Name the parasite shown.
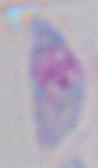
This is Toxoplasma gondii.

Summary:
  - Magnification: 1000x
  - Modality: micrograph